State the preparation type.
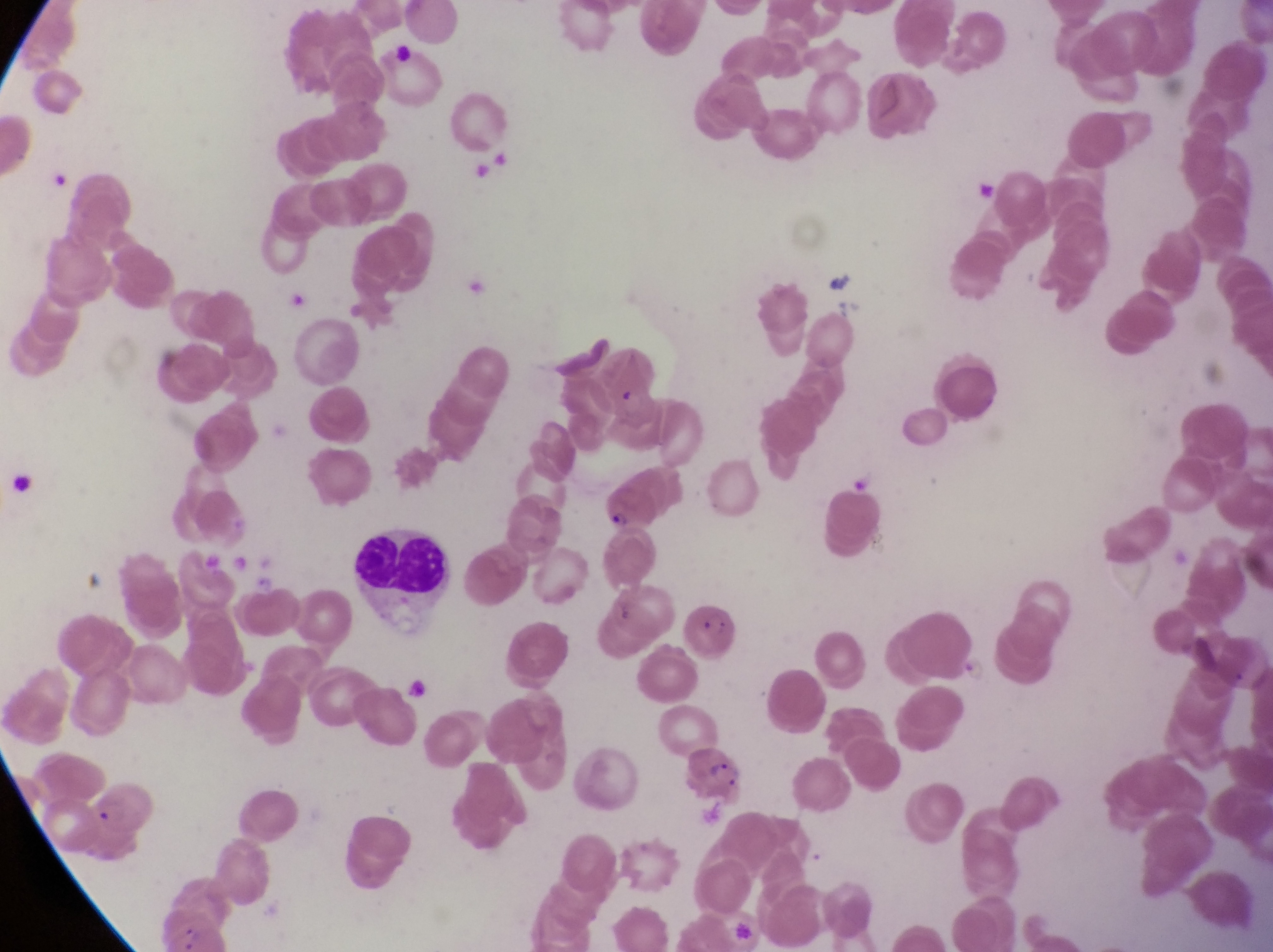
Thin blood smear.

{
  "image_size": "1273×952 pixels",
  "magnification": "1000x",
  "parasitised_red_blood_cell_locations": "approximate bounding boxes as [left, top, right, bottom] in pixels: [597, 485, 660, 540], [679, 596, 741, 661], [682, 746, 754, 809]",
  "artifact_platelet_like_body_stain_precipitate_or_debris_locations": "approximate bounding boxes as [left, top, right, bottom] in pixels: [966, 172, 1005, 207], [829, 299, 869, 327]",
  "capture": "smartphone photograph through the eyepiece of an Olympus CX-23 microscope",
  "leukocyte_locations": "approximate bounding boxes as [left, top, right, bottom] in pixels: [342, 527, 454, 629]",
  "field_of_view": "single",
  "country": "Uganda",
  "trophozoite_locations": "approximate bounding boxes as [left, top, right, bottom] in pixels: [956, 659, 995, 691]"
}